Outline each blood parasite and name the species.
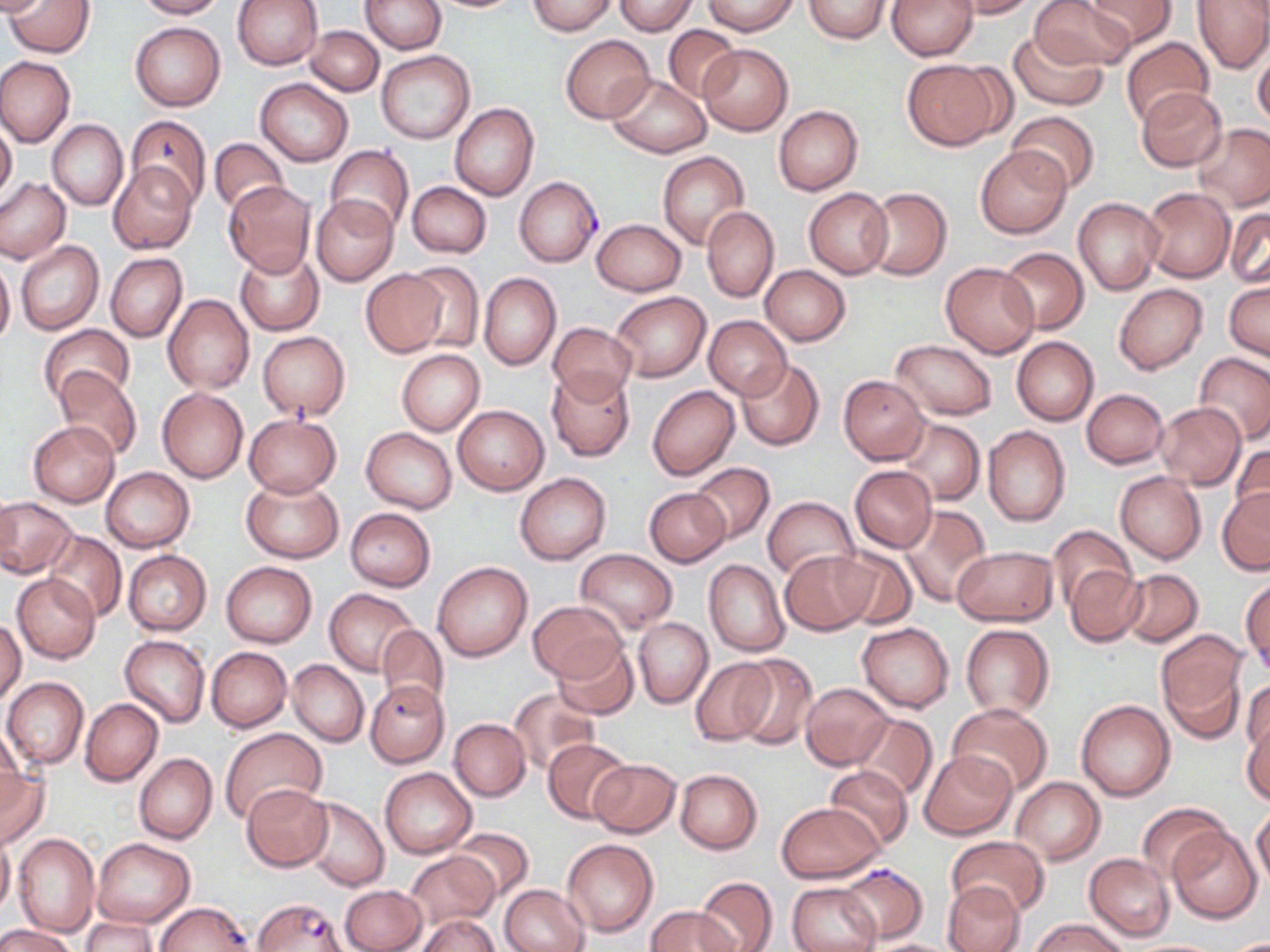

Approximate bounding boxes as (x1,y1)-(x2,y2) corner pairs in pixels.
Plasmodium falciparum-infected red blood cells: (514,177)-(602,266), (377,625)-(449,720), (835,863)-(932,945), (252,898)-(350,952).
No Plasmodium ovale, Plasmodium malariae, Plasmodium vivax, Babesia divergens, or Trypanosoma brucei observed.

slide-level diagnosis = Plasmodium falciparum
magnification = 1000x
uninfected red blood cell locations = approximate bounding boxes as (x1,y1)-(x2,y2) corner pairs in pixels: (136,0)-(226,19), (233,0)-(323,69), (360,0)-(447,53), (529,0)-(615,35), (803,0)-(893,41), (887,0)-(978,60), (951,0)-(1036,18), (1028,0)-(1136,70), (1087,0)-(1176,47), (1191,0)-(1270,73), (6,1)-(95,57), (612,1)-(698,35), (702,1)-(798,35), (130,22)-(225,110), (306,25)-(383,95), (663,26)-(740,101), (1008,29)-(1109,110), (561,34)-(654,121), (1120,37)-(1216,128), (697,44)-(794,134), (1252,44)-(1270,129), (377,49)-(474,143), (0,56)-(75,147), (903,60)-(1001,149), (606,75)-(711,158), (257,78)-(352,166), (1135,88)-(1227,172), (451,104)-(539,201), (773,105)-(864,195), (1007,110)-(1102,194), (126,115)-(211,208), (0,119)-(17,201), (47,119)-(128,210), (1194,123)-(1270,210), (209,137)-(289,216), (975,145)-(1070,238), (326,146)-(414,235), (658,151)-(749,250), (109,161)-(198,255), (0,177)-(70,264), (224,181)-(317,277), (407,182)-(491,257), (804,187)-(893,278), (863,187)-(951,280), (1140,187)-(1234,282), (312,194)-(397,286), (1074,198)-(1163,295), (1226,206)-(1269,290), (701,207)-(778,302), (591,219)-(686,296), (16,241)-(104,337), (234,245)-(326,336), (998,247)-(1090,333), (106,253)-(188,342), (0,256)-(15,347), (404,260)-(484,354), (941,262)-(1040,357), (760,265)-(851,345), (360,269)-(448,357), (479,273)-(561,370), (1225,281)-(1269,361), (1114,283)-(1208,374), (612,292)-(711,381), (163,294)-(255,394), (704,316)-(792,400), (547,322)-(636,403), (38,324)-(136,409), (258,332)-(350,420), (1011,336)-(1098,426), (891,339)-(997,419), (397,349)-(485,436), (1195,353)-(1270,444), (736,360)-(825,452), (547,367)-(634,461), (54,368)-(142,461), (838,374)-(930,464), (648,385)-(740,481), (157,388)-(247,483), (1082,388)-(1169,469), (1153,402)-(1247,489), (453,405)-(549,495), (243,412)-(342,498), (896,417)-(984,506), (28,420)-(119,507), (983,425)-(1070,525), (361,428)-(457,513), (1229,443)-(1269,528), (689,463)-(775,544), (849,466)-(936,553), (100,467)-(193,553), (1115,471)-(1206,564), (515,472)-(612,565), (241,474)-(344,563), (1217,486)-(1269,574), (642,487)-(730,567), (0,497)-(77,578), (761,497)-(859,579), (898,505)-(991,607), (345,507)-(436,590), (1048,527)-(1135,614), (43,531)-(128,623), (829,546)-(916,629), (952,546)-(1055,625), (123,549)-(212,635), (576,549)-(678,634), (780,550)-(875,636), (704,558)-(789,657), (222,560)-(316,646), (433,560)-(533,663), (1066,566)-(1146,647), (1119,568)-(1203,646), (12,573)-(100,664), (1242,580)-(1269,673), (324,589)-(419,675), (529,599)-(624,683), (0,618)-(25,707), (634,618)-(712,706), (856,621)-(954,712), (960,623)-(1055,720), (1157,631)-(1250,737), (119,634)-(210,727), (553,640)-(640,720), (206,647)-(292,732), (732,654)-(819,751), (692,658)-(775,744), (286,659)-(368,747), (2,677)-(88,771), (1242,678)-(1268,764), (800,682)-(893,770), (369,685)-(448,771), (508,689)-(599,775), (81,698)-(163,785), (1076,700)-(1175,801), (948,704)-(1054,796), (849,714)-(938,801), (1242,716)-(1270,805), (449,719)-(530,800), (1,726)-(24,817), (220,728)-(328,820), (543,738)-(632,824), (920,749)-(1017,838), (134,752)-(217,845), (589,759)-(681,838), (824,765)-(913,852), (0,766)-(49,850), (380,767)-(477,858), (675,769)-(761,855), (1010,777)-(1104,865), (241,784)-(332,872), (303,797)-(388,891), (776,801)-(883,883), (1138,802)-(1229,883), (1252,808)-(1270,887), (1168,826)-(1262,923), (452,828)-(533,900), (0,829)-(14,920), (14,834)-(100,937), (946,836)-(1048,917), (92,838)-(196,928), (562,838)-(658,936), (404,850)-(501,930), (1085,853)-(1174,941), (695,877)-(777,952), (786,880)-(882,952), (942,880)-(1025,952), (340,885)-(426,952), (499,885)-(589,952), (646,905)-(740,952), (417,915)-(499,952), (81,917)-(157,950), (1032,918)-(1128,952), (0,923)-(78,952), (862,939)-(960,952)
image size = 1270×952 pixels
preparation = thin blood film
field of view = one of a larger specimen
stain = May-Grünwald-Giemsa
modality = optical microscopy